Name the blood parasite species.
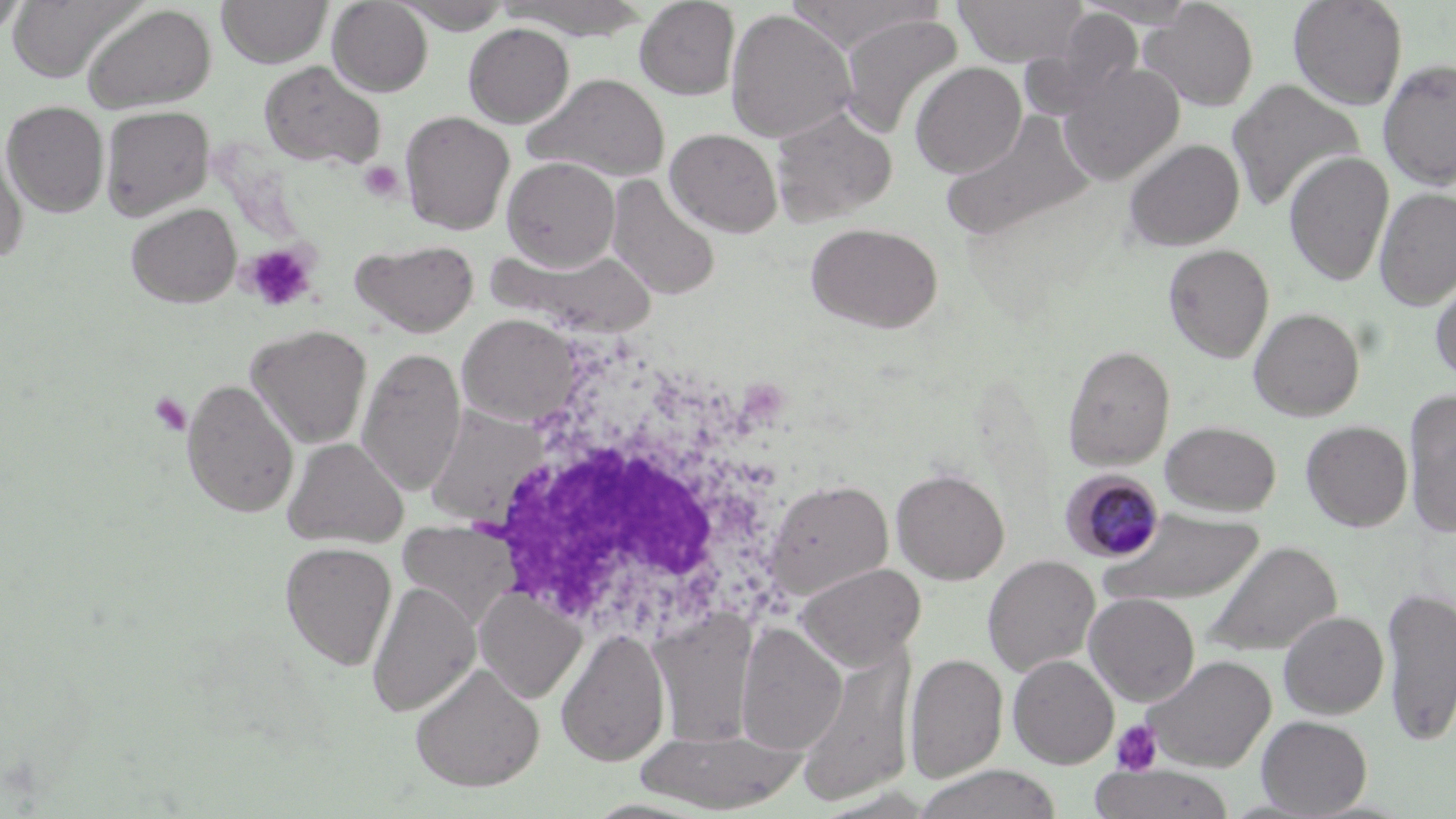

Plasmodium malariae.

stain = May-Grünwald-Giemsa
magnification = 1000x
white blood cell locations = approximate bounding boxes as (x1,y1)-(x2,y2) corner pairs in pixels: (489,415)-(796,633)
uninfected red blood cell locations = approximate bounding boxes as (x1,y1)-(x2,y2) corner pairs in pixels: (0,0)-(31,40), (6,0)-(144,83), (216,0)-(333,68), (634,0)-(741,100), (784,0)-(941,51), (953,0)-(1089,66), (1075,0)-(1202,27), (1141,0)-(1259,112), (1288,0)-(1409,110), (327,1)-(433,96), (394,1)-(513,33), (498,1)-(651,40), (82,4)-(218,113), (725,9)-(856,144), (1026,9)-(1145,116), (836,14)-(964,138), (463,23)-(574,127), (1378,58)-(1456,190), (258,60)-(386,170), (910,62)-(1027,179), (1057,62)-(1184,185), (525,73)-(670,182), (1227,79)-(1366,214), (1,100)-(109,217), (100,105)-(215,220), (769,107)-(897,225), (399,110)-(515,235), (941,111)-(1097,243), (665,128)-(783,237), (0,137)-(29,265), (1123,138)-(1245,251), (1283,152)-(1394,286), (502,157)-(620,271), (606,175)-(722,301), (1374,187)-(1456,310), (126,203)-(242,308), (806,222)-(943,333), (351,238)-(480,338), (485,244)-(656,337), (1163,244)-(1274,362), (1430,274)-(1456,383), (1248,308)-(1365,421), (457,314)-(582,427), (245,325)-(373,449), (1062,344)-(1175,470), (357,347)-(466,496), (182,378)-(299,518), (1404,391)-(1456,537), (424,403)-(549,527), (1160,420)-(1282,516), (1301,420)-(1413,531), (282,437)-(409,548), (892,468)-(1010,584), (766,479)-(894,600), (1099,510)-(1265,607), (398,523)-(520,631), (1202,541)-(1341,658), (280,542)-(398,670), (983,555)-(1100,676), (794,562)-(926,670), (367,580)-(480,717), (474,586)-(587,703), (1381,586)-(1455,745), (1084,593)-(1201,706), (651,610)-(758,747), (1278,611)-(1389,719), (736,622)-(846,754), (556,628)-(671,768), (793,646)-(915,810), (904,654)-(1007,782), (1008,654)-(1119,768), (1143,655)-(1276,772), (410,663)-(545,792), (1257,715)-(1372,817), (633,725)-(809,812), (912,765)-(1068,819), (1088,765)-(1237,819)
Plasmodium malariae-infected red blood cell locations = approximate bounding boxes as (x1,y1)-(x2,y2) corner pairs in pixels: (1061,469)-(1166,562)
platelet locations = approximate bounding boxes as (x1,y1)-(x2,y2) corner pairs in pixels: (359,161)-(404,203), (241,243)-(318,312), (148,392)-(192,436), (1110,719)-(1163,775)
modality = optical microscopy
field of view = one of a larger specimen
image size = 1456×819 pixels
preparation = thin blood film